Name the blood parasite species.
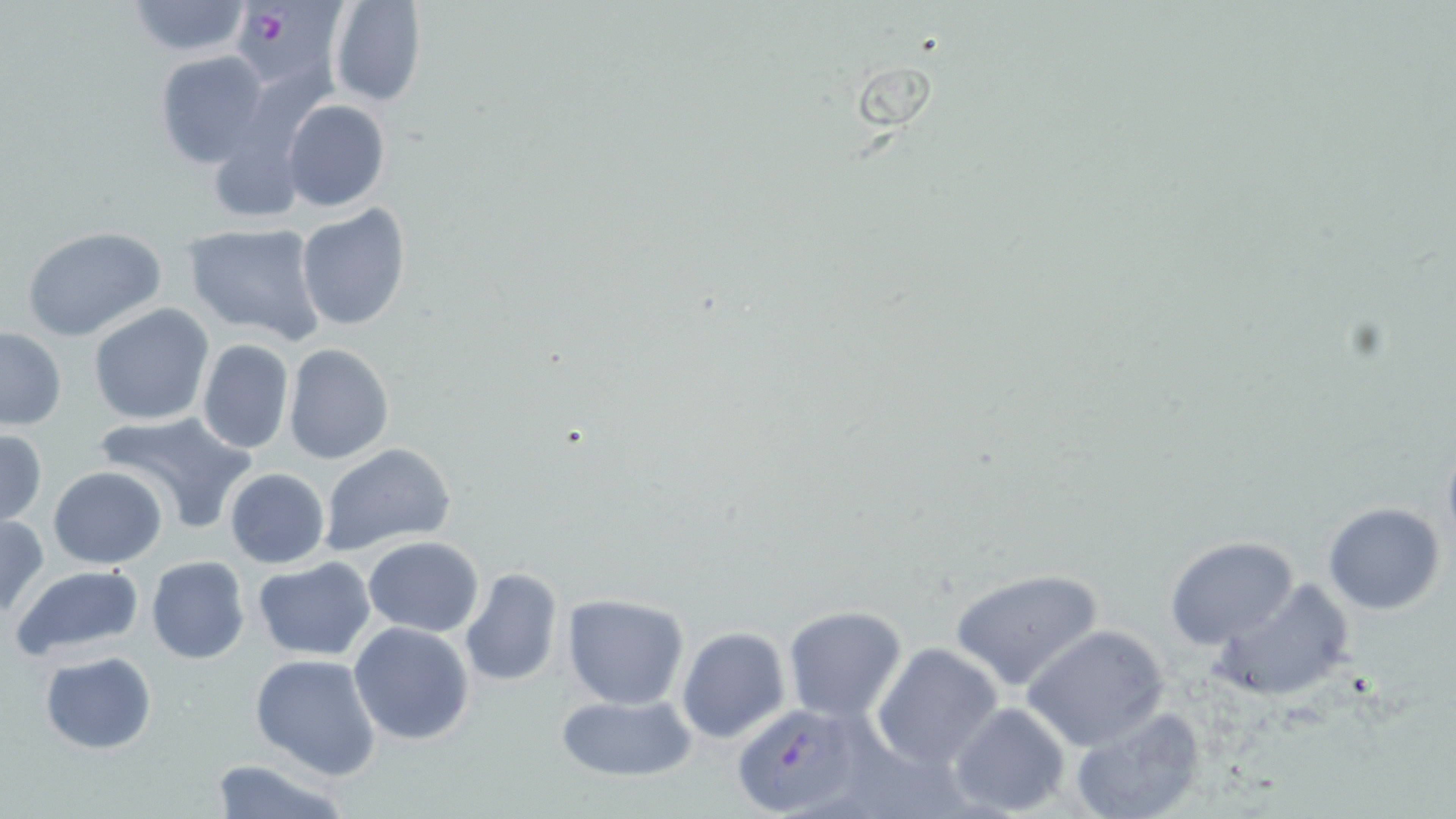
Plasmodium falciparum.

Summary:
  - Coordinate format: approximate bounding boxes as (x1, y1, x2, y2) in pixels
  - Uninfected red blood cell locations: (327, 0, 426, 107), (125, 1, 252, 56), (154, 50, 268, 168), (283, 100, 390, 213), (209, 133, 308, 223), (296, 203, 412, 333), (181, 222, 327, 346), (23, 226, 166, 341), (87, 303, 215, 426), (0, 328, 67, 432), (197, 340, 295, 454), (283, 344, 394, 464), (95, 412, 256, 532), (0, 429, 48, 527), (1441, 441, 1456, 554), (318, 443, 456, 554), (47, 465, 168, 568), (224, 468, 330, 568), (1324, 502, 1445, 614), (0, 515, 48, 618), (363, 535, 484, 637), (1164, 537, 1299, 648), (147, 555, 251, 665), (252, 558, 376, 660), (11, 563, 145, 661), (459, 567, 564, 689), (950, 567, 1106, 693), (1209, 576, 1354, 700), (561, 593, 691, 709), (783, 604, 909, 721), (348, 622, 475, 747), (1021, 623, 1170, 750), (676, 627, 790, 744), (872, 641, 1004, 770), (40, 651, 157, 753), (249, 652, 381, 779), (552, 691, 702, 782), (949, 702, 1072, 817), (1070, 705, 1206, 818), (209, 756, 351, 819)
  - Plasmodium falciparum-infected red blood cell locations: (237, 1, 351, 90), (733, 703, 861, 814)
  - Field of view: one of a larger specimen
  - Preparation: thin blood film
  - Image size: 1456×819 pixels
  - Stain: May-Grünwald-Giemsa
  - Modality: optical microscopy
  - Magnification: 1000x